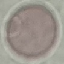
Result: no malaria parasites seen. Giemsa-stained preparation. Cell patch, automatically extracted from a larger field of view and resized to 64 × 64 pixels. Thin blood film. Acquired by smartphone through the microscope eyepiece.